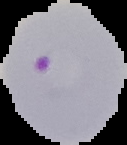

Cell region segmented out of the field of view; the surrounding area is masked to black. From a thin blood smear. Image is 127×145 pixels. Result: malaria parasites identified.